Report the malaria status of this cell.
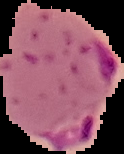
It is parasitized.

{
  "preparation": "thin blood smear",
  "image_size": "124×154 pixels",
  "image_type": "segmented cell region on a black background"
}